Identify the parasite.
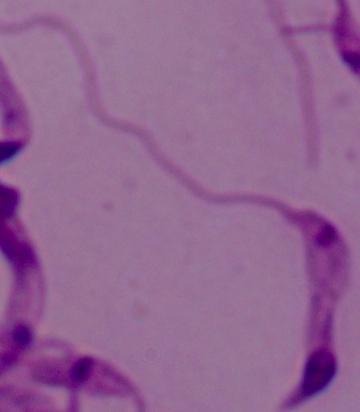
This is Leishmania.

Summary:
  - Modality: micrograph
  - Magnification: 1000x